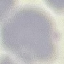
{
  "malaria_status": "uninfected",
  "image_type": "automatically extracted cell patch, resized to 64 × 64 pixels",
  "capture": "smartphone through the microscope eyepiece",
  "preparation": "thin smear",
  "stain": "Giemsa"
}